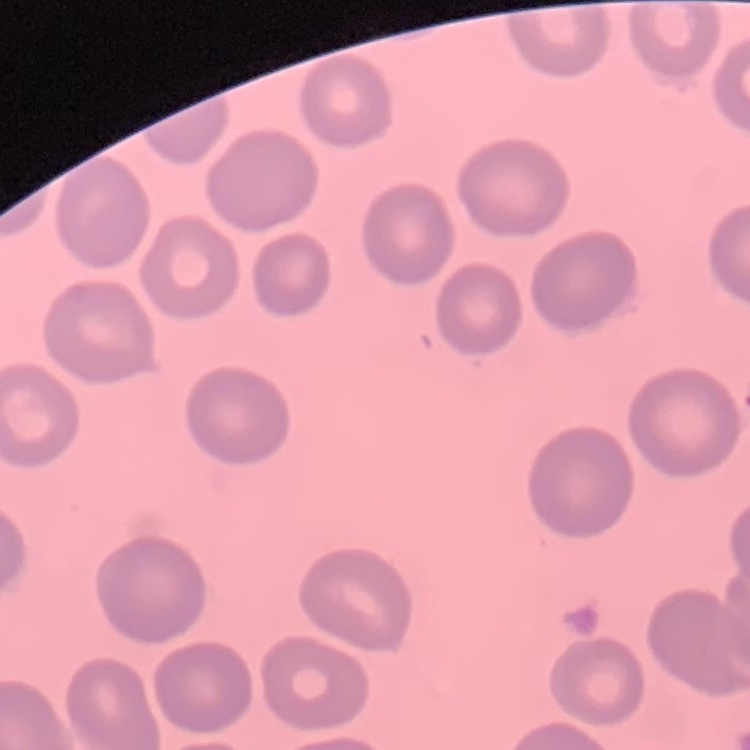

red blood cell morphology = no rouleaux formation
image type = square crop of a larger photomicrograph
stain = Field's or Giemsa
preparation = thin blood smear